Outline every malaria parasite, every leukocyte, and every artifact (stain precipitate or debris).
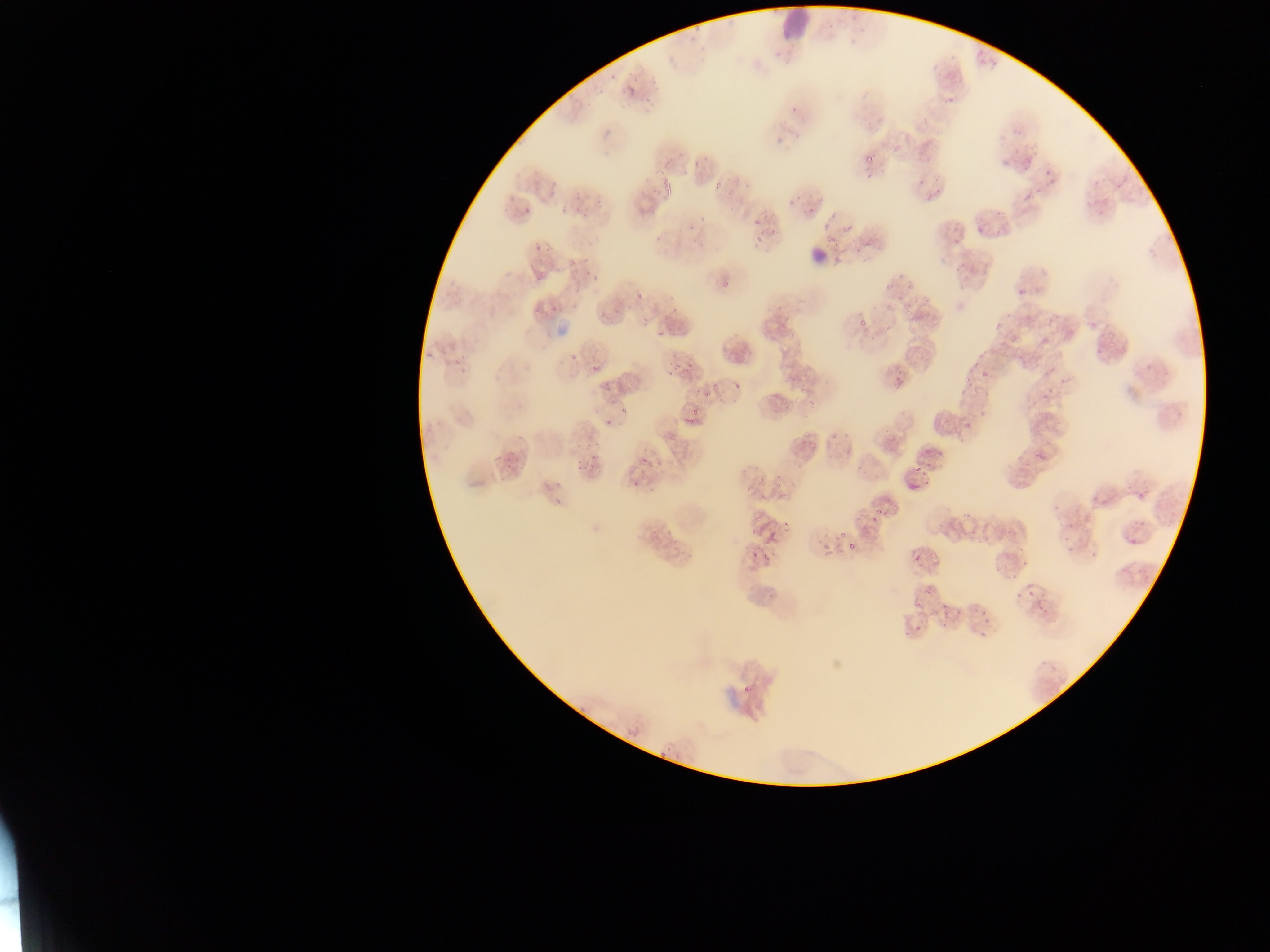

Approximate bounding boxes as {left, top, right, bottom} in pixels.
Malaria parasites: {606, 71, 618, 80}, {652, 71, 659, 88}, {630, 80, 637, 94}, {624, 94, 634, 101}, {639, 96, 655, 105}, {864, 153, 875, 163}, {546, 178, 556, 192}, {662, 178, 672, 190}, {714, 179, 727, 191}, {522, 205, 531, 215}, {569, 205, 583, 213}, {698, 216, 706, 224}, {750, 217, 764, 229}, {769, 228, 782, 235}, {752, 232, 765, 250}, {653, 235, 667, 245}, {532, 243, 542, 256}, {563, 256, 577, 272}, {583, 257, 593, 263}, {586, 274, 597, 280}, {719, 277, 734, 289}, {904, 282, 918, 292}, {634, 287, 646, 299}, {666, 293, 677, 301}, {570, 299, 579, 312}, {549, 302, 563, 311}, {668, 307, 682, 315}, {903, 307, 914, 319}, {640, 316, 650, 326}, {1023, 316, 1034, 324}, {858, 317, 868, 327}, {881, 321, 890, 332}, {657, 324, 667, 336}, {1011, 332, 1024, 345}, {912, 334, 921, 345}, {1095, 340, 1113, 358}, {666, 349, 679, 357}, {722, 350, 730, 363}, {568, 352, 577, 361}, {974, 353, 984, 360}, {454, 357, 465, 367}, {684, 360, 695, 372}, {968, 361, 985, 366}, {1144, 361, 1154, 369}, {803, 363, 815, 376}, {669, 365, 677, 374}, {588, 366, 604, 373}, {977, 368, 989, 383}, {960, 373, 974, 387}, {599, 376, 615, 393}, {733, 382, 739, 391}, {702, 387, 713, 397}, {780, 397, 789, 407}, {616, 402, 628, 415}, {689, 405, 703, 417}, {776, 405, 785, 412}, {1174, 405, 1184, 419}, {682, 416, 696, 427}, {603, 419, 614, 428}, {959, 423, 971, 434}, {799, 439, 807, 447}, {577, 443, 594, 454}, {1015, 448, 1026, 463}, {1033, 448, 1045, 458}, {489, 454, 506, 469}, {589, 455, 599, 463}, {580, 457, 605, 473}, {639, 457, 648, 463}, {503, 458, 514, 469}, {1022, 459, 1032, 477}, {655, 460, 666, 468}, {916, 462, 933, 489}, {550, 477, 567, 489}, {632, 477, 643, 489}, {774, 481, 782, 489}, {543, 483, 551, 494}, {780, 486, 794, 499}, {1137, 488, 1150, 498}, {550, 494, 567, 505}, {1051, 499, 1063, 533}, {890, 504, 900, 514}, {960, 508, 968, 521}, {875, 509, 883, 517}, {1133, 518, 1144, 525}, {782, 522, 793, 532}, {661, 525, 673, 539}, {1003, 528, 1012, 536}, {833, 529, 849, 546}, {968, 530, 976, 536}, {761, 534, 778, 546}, {1126, 535, 1138, 549}, {952, 536, 958, 544}, {1064, 536, 1078, 560}, {671, 541, 682, 555}, {818, 541, 832, 560}, {848, 542, 856, 550}, {1088, 543, 1102, 562}, {932, 548, 940, 566}, {763, 549, 774, 564}, {748, 550, 761, 564}, {681, 553, 693, 560}, {911, 555, 925, 567}, {1022, 560, 1030, 567}, {991, 565, 1001, 572}, {1005, 571, 1016, 583}, {924, 585, 932, 596}, {1027, 589, 1035, 597}, {1016, 591, 1023, 602}, {1036, 596, 1052, 615}, {911, 599, 925, 610}, {941, 609, 951, 618}, {979, 610, 989, 623}, {940, 623, 947, 631}, {915, 624, 923, 633}, {977, 631, 985, 644}, {741, 685, 753, 698}, {625, 718, 642, 744}, {664, 746, 680, 754}, {655, 751, 665, 759} | approximate {x, y} pixel centers of objects too small to bound: {960, 527}, {945, 605}.
Leukocytes: {776, 0, 821, 40}, {804, 241, 832, 267}.

Image is 1270×952 pixels. Mobile-phone photograph taken through the microscope. One field of view. Thin blood smear. Collected in Ghana.